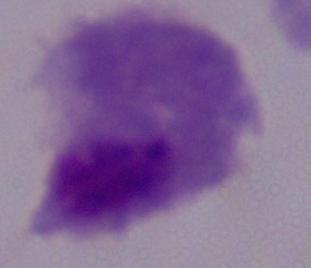

Summary:
  - Magnification: 1000x
  - Identification: trichomonad
  - Modality: micrograph